Locate every blood parasite and identify its species.
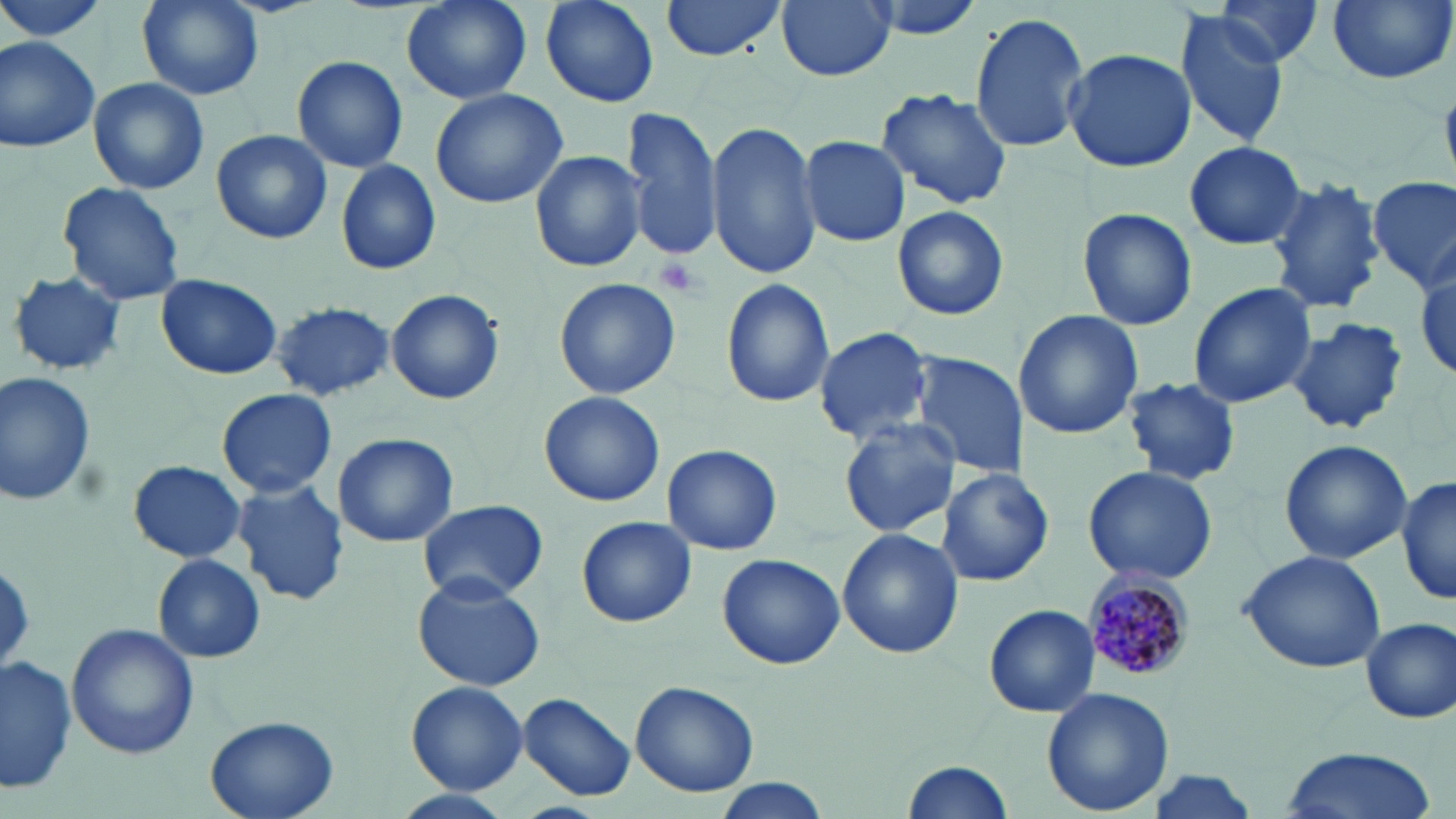

Approximate bounding boxes as (x1, y1, x2, y2) in pixels.
Plasmodium malariae-infected red blood cells: (1081, 573, 1193, 684).
No Plasmodium falciparum, Plasmodium ovale, Plasmodium vivax, Babesia divergens, or Trypanosoma brucei observed.

Uninfected red blood cell locations: (400, 0, 533, 105), (539, 0, 659, 108), (660, 0, 790, 62), (777, 0, 895, 81), (859, 0, 990, 42), (1324, 0, 1454, 86), (136, 1, 262, 101), (1214, 1, 1322, 69), (1173, 9, 1292, 149), (968, 11, 1090, 155), (0, 34, 102, 153), (1063, 49, 1196, 174), (292, 55, 409, 173), (88, 77, 210, 196), (429, 86, 571, 209), (875, 88, 1011, 210), (623, 108, 723, 264), (705, 119, 820, 280), (211, 129, 332, 244), (801, 136, 910, 246), (1183, 140, 1308, 250), (530, 150, 648, 273), (334, 158, 443, 276), (1265, 176, 1387, 316), (1366, 177, 1455, 291), (56, 180, 186, 307), (892, 206, 1009, 321), (1077, 209, 1197, 330), (1411, 255, 1456, 381), (8, 270, 125, 377), (156, 273, 282, 380), (553, 279, 682, 400), (721, 280, 834, 408), (1188, 283, 1317, 407), (384, 288, 506, 405), (269, 300, 395, 402), (1014, 310, 1143, 438), (1284, 317, 1408, 434), (812, 325, 938, 447), (910, 354, 1028, 480), (0, 372, 95, 510), (1125, 377, 1241, 487), (216, 388, 337, 499), (540, 391, 664, 507), (840, 417, 960, 537), (332, 431, 460, 548), (1278, 438, 1412, 566), (662, 443, 782, 555), (128, 459, 247, 564), (1082, 465, 1218, 585), (936, 468, 1057, 587), (232, 477, 350, 607), (1395, 477, 1454, 607), (417, 499, 548, 604), (576, 515, 696, 628), (838, 528, 963, 659), (1239, 550, 1387, 674), (717, 553, 844, 670), (153, 554, 265, 663), (412, 575, 546, 692), (984, 604, 1099, 717), (1360, 617, 1455, 724), (67, 621, 198, 758), (3, 655, 78, 796), (628, 680, 759, 798), (406, 682, 527, 795), (1043, 687, 1176, 815), (518, 691, 637, 803), (206, 714, 340, 819), (1280, 744, 1435, 819), (901, 756, 1014, 819), (1134, 768, 1270, 817), (713, 779, 830, 817), (383, 790, 517, 819). Platelet locations: (652, 256, 708, 298). Slide-level diagnosis: Plasmodium malariae. Captured at 1000x magnification. Image is 1456×819 pixels. Light microscopy. Thin blood film. May-Grünwald-Giemsa-stained preparation. One field of a larger specimen.